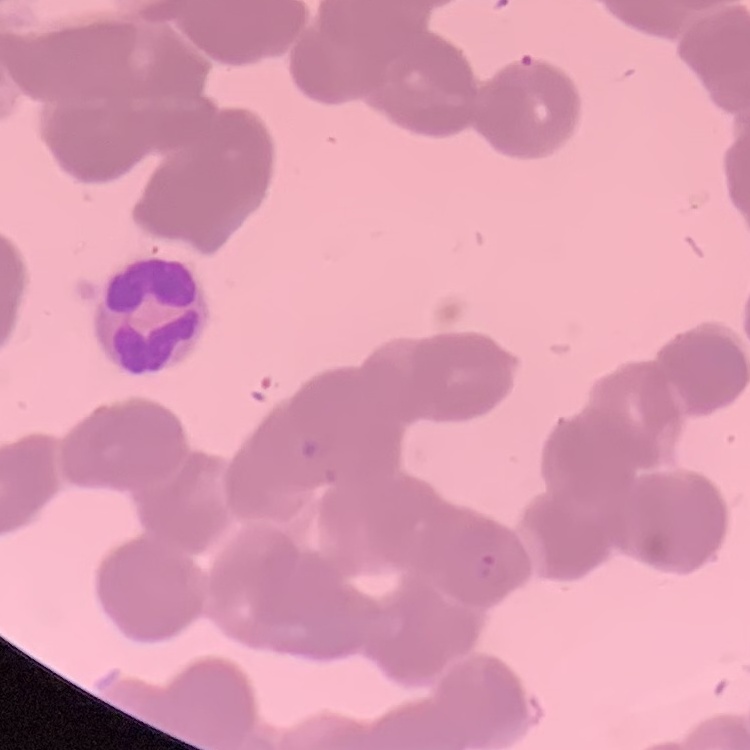

Summary:
  - Erythrocyte morphology: rouleaux formation
  - Preparation: thin blood smear
  - Stain: Field's or Giemsa
  - Image type: square crop of a larger photomicrograph